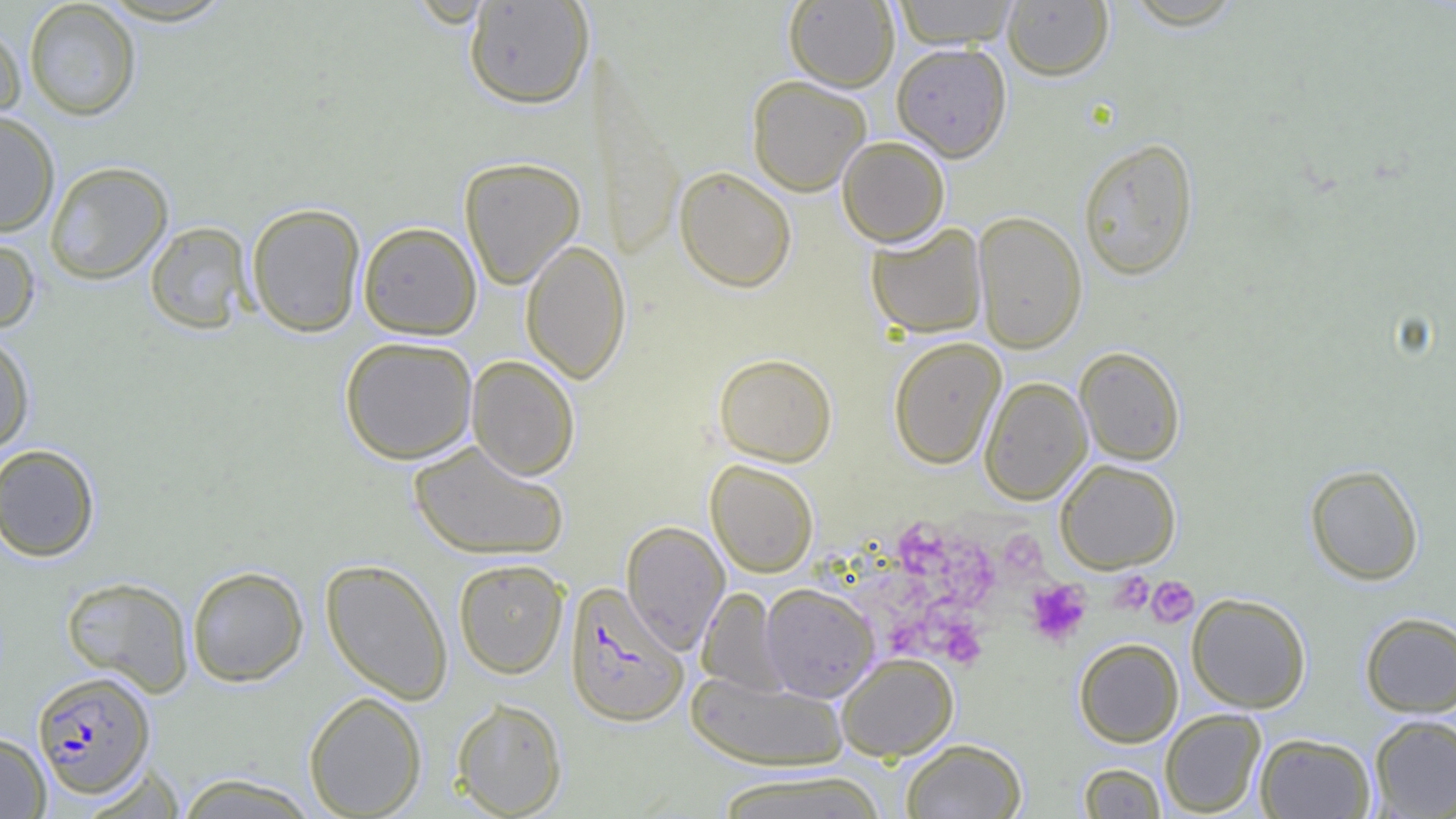 Approximate bounding boxes as named x1/y1/x2/y2 corners in pixels. Uninfected red blood cell locations: (x1=892, y1=0, x2=1019, y2=48), (x1=23, y1=1, x2=141, y2=121), (x1=463, y1=1, x2=594, y2=110), (x1=784, y1=1, x2=899, y2=91), (x1=1002, y1=1, x2=1114, y2=81), (x1=0, y1=20, x2=25, y2=128), (x1=891, y1=42, x2=1012, y2=161), (x1=747, y1=76, x2=871, y2=196), (x1=0, y1=111, x2=60, y2=236), (x1=837, y1=135, x2=950, y2=247), (x1=1078, y1=138, x2=1199, y2=281), (x1=459, y1=156, x2=586, y2=290), (x1=44, y1=161, x2=173, y2=285), (x1=674, y1=165, x2=797, y2=292), (x1=246, y1=202, x2=366, y2=337), (x1=972, y1=210, x2=1087, y2=354), (x1=145, y1=221, x2=254, y2=335), (x1=358, y1=221, x2=482, y2=340), (x1=866, y1=222, x2=988, y2=338), (x1=0, y1=228, x2=41, y2=333), (x1=520, y1=239, x2=631, y2=384), (x1=0, y1=331, x2=35, y2=454), (x1=339, y1=336, x2=478, y2=464), (x1=888, y1=337, x2=1006, y2=469), (x1=1075, y1=346, x2=1186, y2=465), (x1=713, y1=353, x2=837, y2=466), (x1=466, y1=355, x2=580, y2=480), (x1=979, y1=376, x2=1092, y2=504), (x1=408, y1=439, x2=569, y2=561), (x1=0, y1=444, x2=101, y2=562), (x1=1054, y1=458, x2=1181, y2=573), (x1=706, y1=460, x2=818, y2=577), (x1=1305, y1=463, x2=1424, y2=585), (x1=622, y1=520, x2=730, y2=655), (x1=320, y1=558, x2=453, y2=704), (x1=453, y1=558, x2=569, y2=679), (x1=187, y1=565, x2=309, y2=687), (x1=61, y1=576, x2=194, y2=695), (x1=760, y1=583, x2=879, y2=702), (x1=697, y1=587, x2=786, y2=696), (x1=1187, y1=593, x2=1311, y2=713), (x1=1359, y1=612, x2=1456, y2=717), (x1=1073, y1=638, x2=1184, y2=747), (x1=836, y1=653, x2=959, y2=761), (x1=687, y1=672, x2=848, y2=771), (x1=303, y1=691, x2=427, y2=818), (x1=452, y1=698, x2=568, y2=818), (x1=1160, y1=709, x2=1266, y2=817), (x1=1369, y1=714, x2=1456, y2=818), (x1=0, y1=732, x2=51, y2=819), (x1=1255, y1=733, x2=1376, y2=818), (x1=900, y1=738, x2=1027, y2=818), (x1=1077, y1=763, x2=1166, y2=818), (x1=81, y1=764, x2=187, y2=818), (x1=714, y1=770, x2=889, y2=818), (x1=174, y1=774, x2=320, y2=818). Plasmodium falciparum-infected red blood cell locations: (x1=565, y1=582, x2=689, y2=727), (x1=32, y1=670, x2=156, y2=798). Platelet locations: (x1=897, y1=526, x2=1000, y2=613), (x1=997, y1=529, x2=1047, y2=581), (x1=1109, y1=571, x2=1154, y2=615), (x1=1146, y1=576, x2=1199, y2=627), (x1=1025, y1=578, x2=1092, y2=647), (x1=885, y1=615, x2=933, y2=658), (x1=936, y1=617, x2=988, y2=670). Slide-level diagnosis: Plasmodium falciparum. Single field of view. Light microscopy. Image is 1456×819 pixels. Thin blood smear. 1000x magnification.